Outline each blood parasite and name the species.
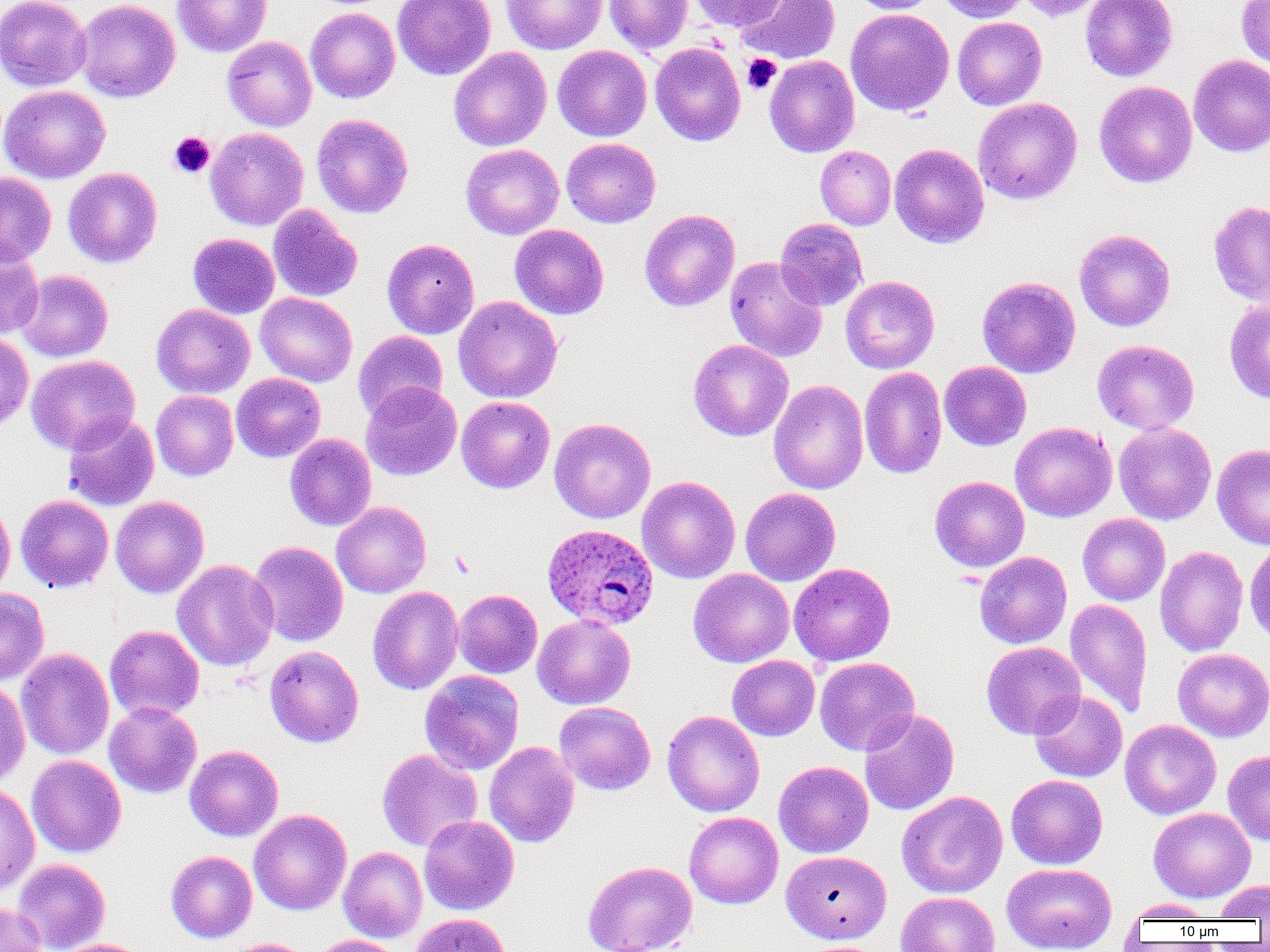

Approximate bounding boxes as named x1/y1/x2/y2 corners in pixels.
Plasmodium ovale-infected red blood cells: (x1=542, y1=523, x2=659, y2=630).
No Plasmodium falciparum, Plasmodium malariae, Plasmodium vivax, Babesia divergens, or Trypanosoma brucei observed.

{
  "slide_level_diagnosis": "Plasmodium ovale",
  "platelet_locations": "approximate bounding boxes as named x1/y1/x2/y2 corners in pixels: (x1=742, y1=54, x2=781, y2=94), (x1=169, y1=132, x2=215, y2=178)",
  "uninfected_red_blood_cell_locations": "approximate bounding boxes as named x1/y1/x2/y2 corners in pixels: (x1=0, y1=0, x2=91, y2=92), (x1=75, y1=0, x2=180, y2=102), (x1=172, y1=0, x2=272, y2=57), (x1=392, y1=0, x2=496, y2=80), (x1=604, y1=0, x2=693, y2=55), (x1=690, y1=0, x2=787, y2=30), (x1=734, y1=0, x2=841, y2=64), (x1=848, y1=0, x2=939, y2=14), (x1=937, y1=0, x2=1030, y2=22), (x1=1015, y1=0, x2=1110, y2=21), (x1=1081, y1=0, x2=1178, y2=81), (x1=1237, y1=0, x2=1270, y2=70), (x1=502, y1=1, x2=606, y2=55), (x1=306, y1=8, x2=400, y2=103), (x1=845, y1=8, x2=955, y2=117), (x1=952, y1=17, x2=1047, y2=110), (x1=222, y1=36, x2=317, y2=132), (x1=650, y1=42, x2=746, y2=146), (x1=552, y1=45, x2=652, y2=141), (x1=449, y1=47, x2=551, y2=152), (x1=1188, y1=54, x2=1270, y2=157), (x1=765, y1=55, x2=859, y2=157), (x1=1094, y1=81, x2=1197, y2=187), (x1=0, y1=84, x2=110, y2=184), (x1=973, y1=97, x2=1082, y2=205), (x1=312, y1=114, x2=413, y2=218), (x1=205, y1=127, x2=308, y2=231), (x1=562, y1=138, x2=660, y2=228), (x1=889, y1=143, x2=989, y2=248), (x1=460, y1=144, x2=564, y2=239), (x1=815, y1=146, x2=896, y2=230), (x1=62, y1=167, x2=162, y2=268), (x1=0, y1=172, x2=56, y2=266), (x1=1209, y1=200, x2=1270, y2=307), (x1=268, y1=204, x2=362, y2=302), (x1=639, y1=209, x2=740, y2=311), (x1=775, y1=218, x2=868, y2=310), (x1=509, y1=224, x2=609, y2=319), (x1=1074, y1=229, x2=1175, y2=331), (x1=188, y1=233, x2=280, y2=319), (x1=382, y1=238, x2=479, y2=339), (x1=0, y1=242, x2=44, y2=339), (x1=725, y1=257, x2=827, y2=362), (x1=16, y1=270, x2=113, y2=362), (x1=840, y1=275, x2=939, y2=373), (x1=977, y1=276, x2=1080, y2=377), (x1=255, y1=292, x2=357, y2=387), (x1=453, y1=296, x2=562, y2=403), (x1=1224, y1=299, x2=1270, y2=403), (x1=151, y1=303, x2=255, y2=399), (x1=353, y1=330, x2=448, y2=422), (x1=0, y1=332, x2=34, y2=434), (x1=688, y1=339, x2=793, y2=441), (x1=1092, y1=340, x2=1200, y2=434), (x1=25, y1=355, x2=140, y2=455), (x1=939, y1=361, x2=1031, y2=451), (x1=859, y1=366, x2=947, y2=479), (x1=231, y1=373, x2=326, y2=462), (x1=768, y1=380, x2=868, y2=494), (x1=360, y1=382, x2=462, y2=481), (x1=151, y1=390, x2=239, y2=481), (x1=457, y1=396, x2=554, y2=493), (x1=62, y1=413, x2=159, y2=511), (x1=549, y1=418, x2=656, y2=524), (x1=1010, y1=422, x2=1117, y2=522), (x1=1114, y1=423, x2=1216, y2=525), (x1=284, y1=433, x2=376, y2=531), (x1=1212, y1=443, x2=1270, y2=549), (x1=637, y1=476, x2=740, y2=584), (x1=930, y1=476, x2=1029, y2=572), (x1=741, y1=487, x2=841, y2=586), (x1=15, y1=495, x2=114, y2=593), (x1=110, y1=495, x2=209, y2=598), (x1=0, y1=499, x2=15, y2=602), (x1=331, y1=501, x2=431, y2=598), (x1=1077, y1=513, x2=1170, y2=605), (x1=249, y1=541, x2=348, y2=647), (x1=1244, y1=541, x2=1270, y2=647), (x1=1155, y1=545, x2=1249, y2=657), (x1=974, y1=551, x2=1072, y2=649), (x1=172, y1=559, x2=278, y2=671), (x1=789, y1=563, x2=896, y2=666), (x1=688, y1=569, x2=795, y2=667), (x1=367, y1=586, x2=463, y2=695), (x1=0, y1=588, x2=49, y2=685), (x1=453, y1=589, x2=542, y2=678), (x1=1065, y1=598, x2=1152, y2=718), (x1=532, y1=614, x2=636, y2=709), (x1=104, y1=625, x2=205, y2=722), (x1=981, y1=642, x2=1086, y2=739), (x1=264, y1=645, x2=364, y2=747), (x1=16, y1=648, x2=114, y2=760), (x1=1173, y1=648, x2=1270, y2=742), (x1=727, y1=655, x2=820, y2=741), (x1=815, y1=657, x2=919, y2=756), (x1=419, y1=670, x2=524, y2=775), (x1=0, y1=682, x2=30, y2=786), (x1=1029, y1=690, x2=1127, y2=782), (x1=554, y1=701, x2=656, y2=795), (x1=104, y1=702, x2=201, y2=799), (x1=859, y1=709, x2=959, y2=816), (x1=662, y1=710, x2=765, y2=817), (x1=1120, y1=719, x2=1221, y2=819), (x1=484, y1=741, x2=579, y2=847), (x1=185, y1=745, x2=283, y2=841), (x1=377, y1=749, x2=483, y2=851), (x1=1222, y1=749, x2=1270, y2=845), (x1=26, y1=755, x2=126, y2=857), (x1=774, y1=761, x2=874, y2=857), (x1=1006, y1=774, x2=1108, y2=869), (x1=0, y1=783, x2=40, y2=895), (x1=897, y1=791, x2=1007, y2=898), (x1=1148, y1=807, x2=1256, y2=902), (x1=249, y1=809, x2=352, y2=915), (x1=684, y1=811, x2=783, y2=909), (x1=418, y1=815, x2=519, y2=915), (x1=338, y1=846, x2=427, y2=942), (x1=165, y1=850, x2=257, y2=943), (x1=781, y1=850, x2=892, y2=944), (x1=12, y1=858, x2=110, y2=952), (x1=583, y1=860, x2=697, y2=952), (x1=1002, y1=862, x2=1117, y2=952), (x1=1214, y1=879, x2=1270, y2=920), (x1=895, y1=891, x2=999, y2=952), (x1=1124, y1=899, x2=1218, y2=922), (x1=0, y1=901, x2=47, y2=952), (x1=412, y1=912, x2=513, y2=952), (x1=310, y1=935, x2=405, y2=952), (x1=56, y1=938, x2=150, y2=952), (x1=223, y1=938, x2=313, y2=952)",
  "field_of_view": "one of a larger specimen",
  "preparation": "thin blood smear",
  "image_size": "1270×952 pixels",
  "modality": "light microscopy",
  "magnification": "1000x"
}